Describe the morphology of the erythrocytes.
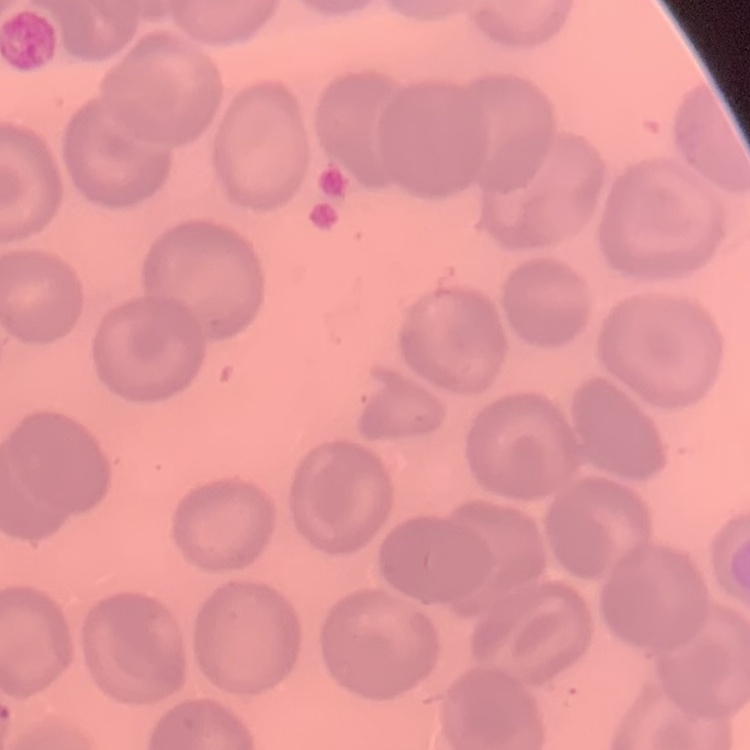

No rouleaux formation.

image type = one tile cut from a larger photomicrograph
preparation = thin peripheral smear
stain = Field's or Giemsa